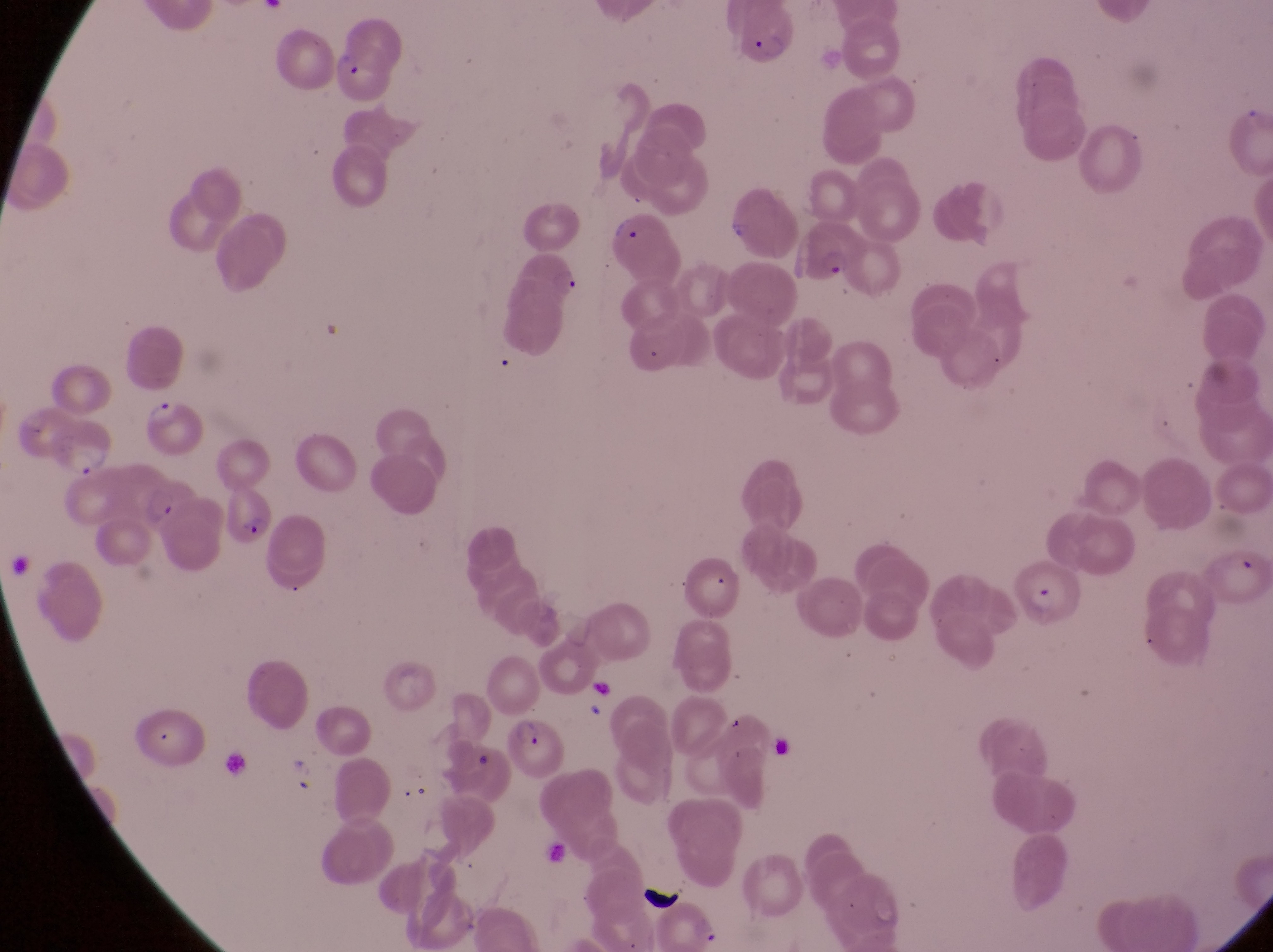

Approximate bounding boxes as [left, top, right, bottom] in pixels.
Summary:
  - Trophozoite locations: [137, 387, 184, 427], [62, 435, 114, 485]
  - Parasitised red blood cell locations: [726, 12, 809, 69], [334, 50, 394, 103], [594, 213, 679, 288], [794, 215, 868, 283], [125, 479, 222, 566], [222, 485, 275, 550], [1019, 565, 1079, 632], [504, 711, 569, 785]
  - Artifact (platelet-like body, stain precipitate, or debris) locations: [721, 213, 749, 243], [591, 675, 623, 708], [637, 876, 684, 915]
  - Country: Uganda
  - Magnification: 1000x
  - Capture: smartphone photograph through the eyepiece of an Olympus CX-23 microscope
  - Image size: 1273×952 pixels
  - Preparation: thin blood smear
  - Field of view: single